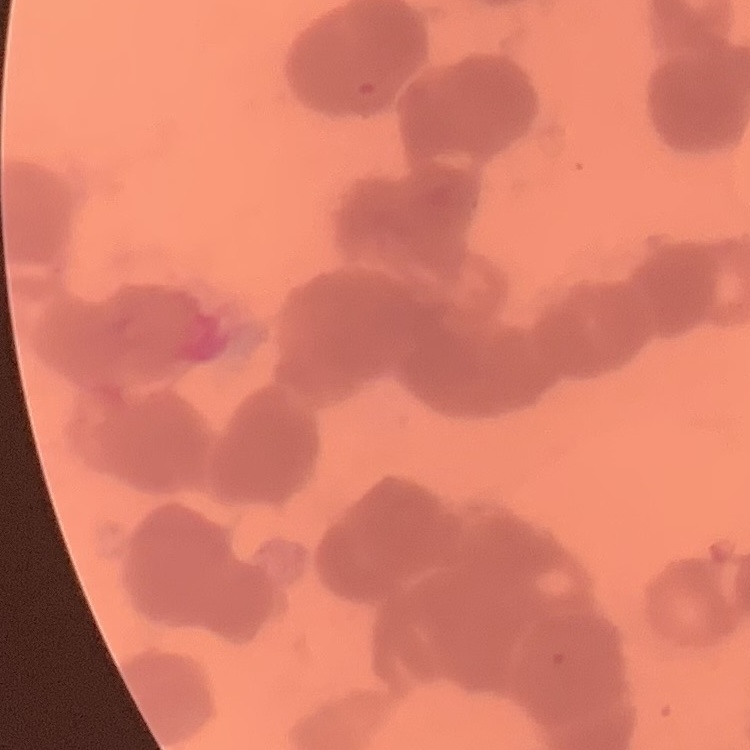
Summary:
  - Red blood cell morphology: rouleaux formation
  - Image type: square crop of a larger photomicrograph
  - Stain: Field's or Giemsa
  - Preparation: thin peripheral smear